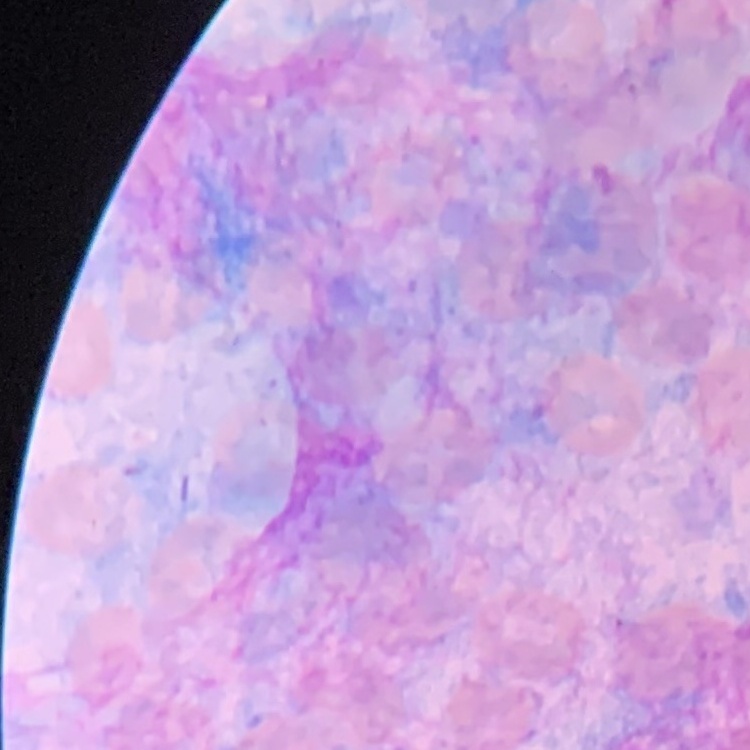
red_blood_cell_morphology: no rouleaux formation
preparation: thin blood film
image_type: square crop of a larger photomicrograph
stain: Field's or Giemsa